State the preparation type.
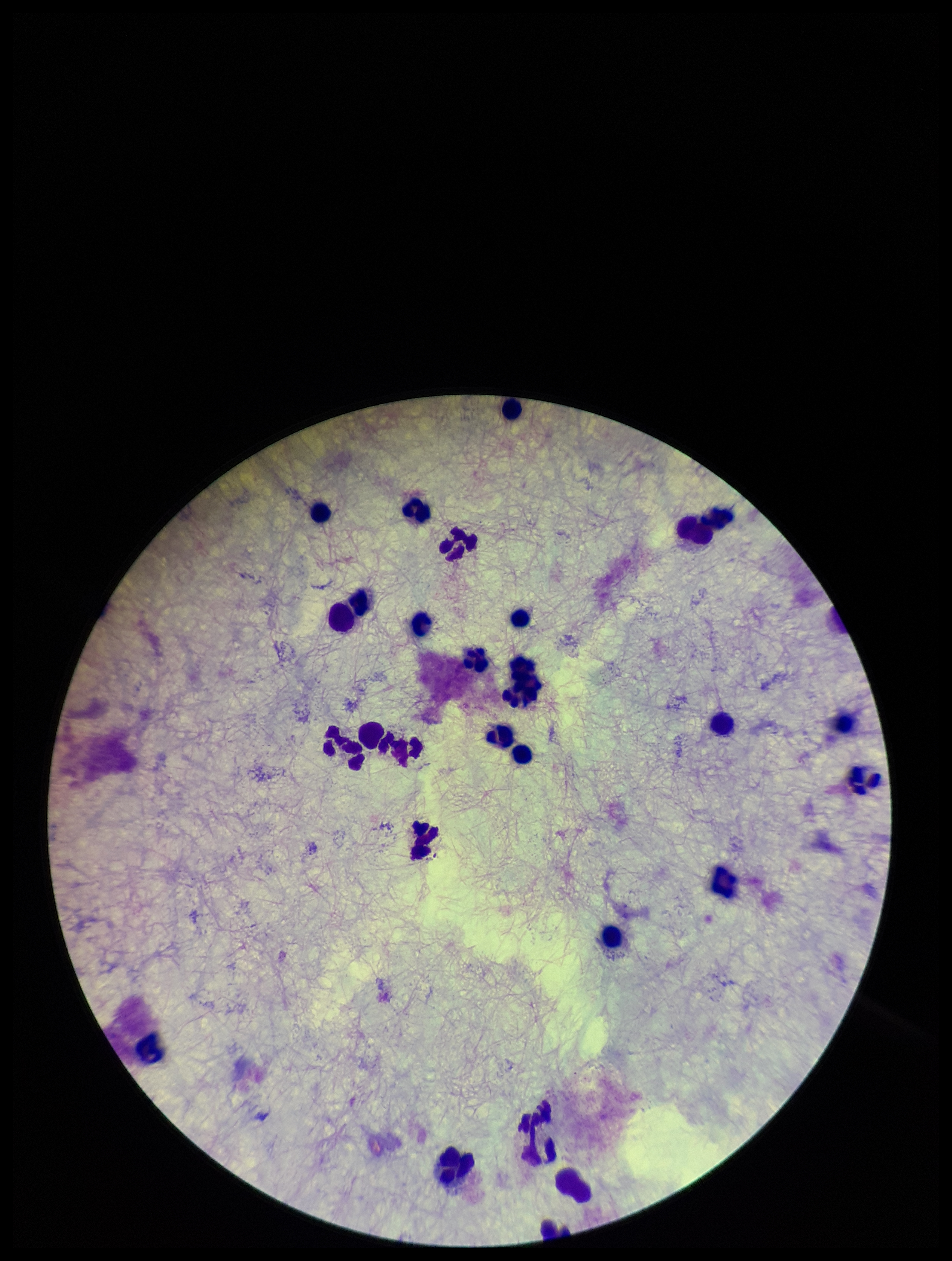
A thick smear.

{
  "patient_malaria_status": "negative",
  "field_of_view": "one from this slide",
  "plasmodium_parasites": "none seen",
  "leukocyte_count": 24,
  "stain": "Giemsa",
  "parasite_count": 0,
  "capture": "smartphone photograph through the microscope eyepiece",
  "image_size": "952×1261 pixels"
}